Assess for parasitized red blood cells.
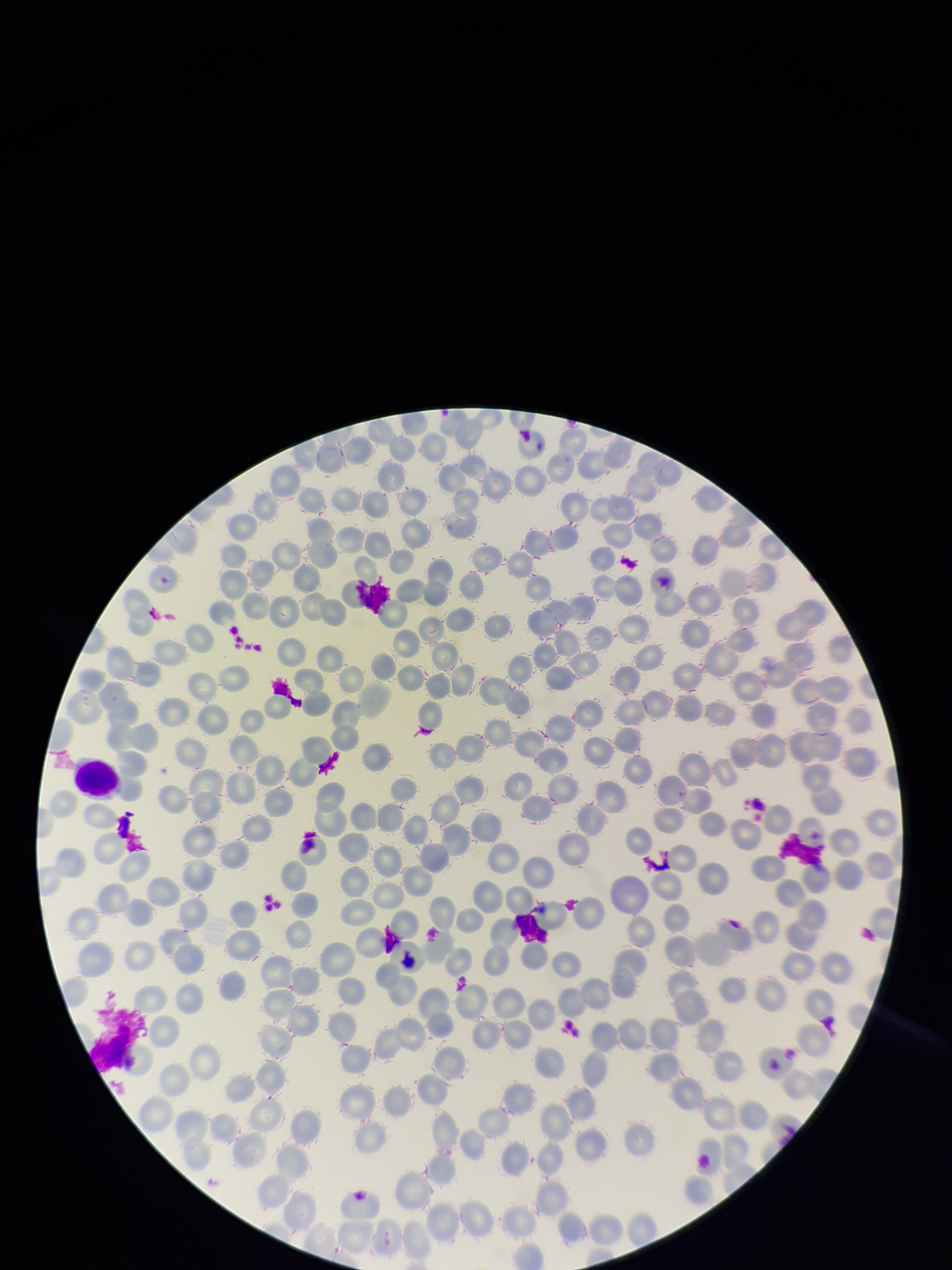
None identified.

parasitized_red_blood_cell_count: 0
image_size: 952×1270 pixels
capture: smartphone photograph through the microscope eyepiece
field_of_view: one from this slide
patient_malaria_status: negative
preparation: thin smear
red_blood_cell_count: 279
stain: Giemsa